Identify the parasite.
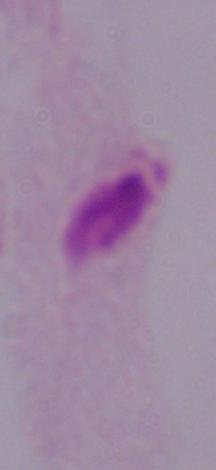

A trichomonad.

Summary:
  - Modality: photomicrograph
  - Magnification: 1000x